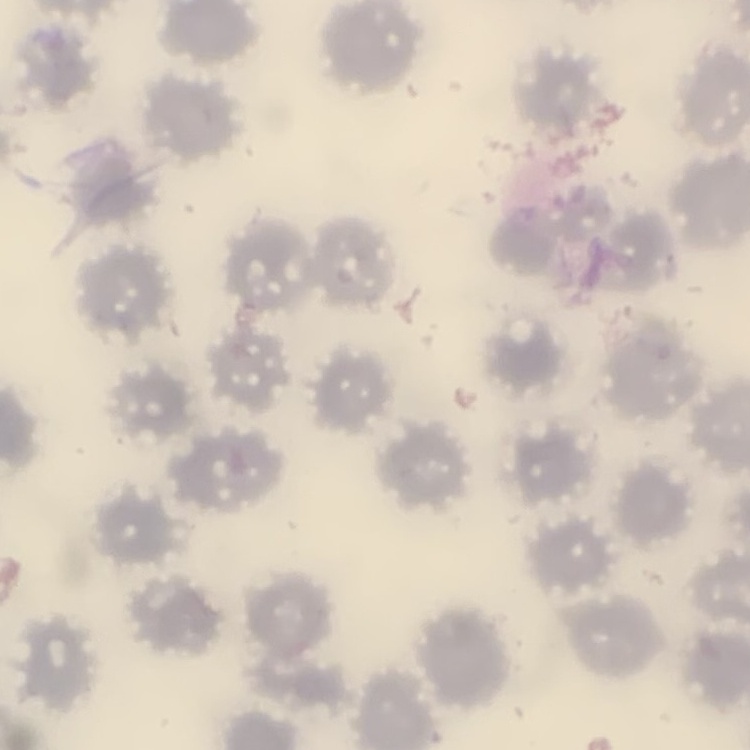
{
  "red_blood_cell_morphology": "no rouleaux formation",
  "preparation": "thin blood smear",
  "stain": "Field's or Giemsa",
  "image_type": "square crop of a larger photomicrograph"
}